Assess the morphology of the red blood cells.
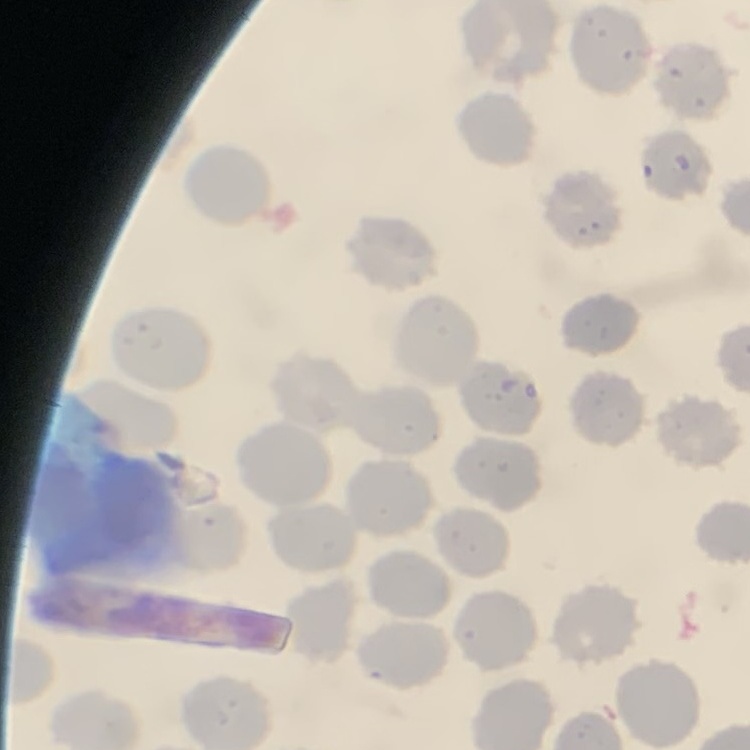

No rouleaux formation.

preparation = thin blood film
image type = one tile cut from a larger photomicrograph
stain = Field's or Giemsa